Describe the morphology of the erythrocytes.
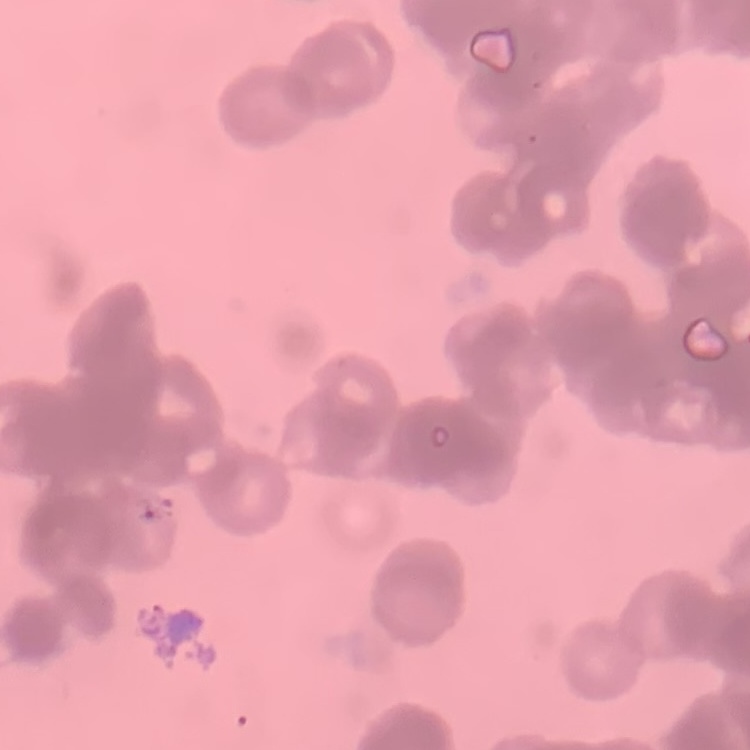
They show rouleaux formation.

Thin blood smear. Field's or Giemsa stain. One tile cut from a larger photomicrograph.